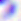
Toxoplasma gondii is seen. 400x magnification. Micrograph.